Locate every blood parasite and identify its species.
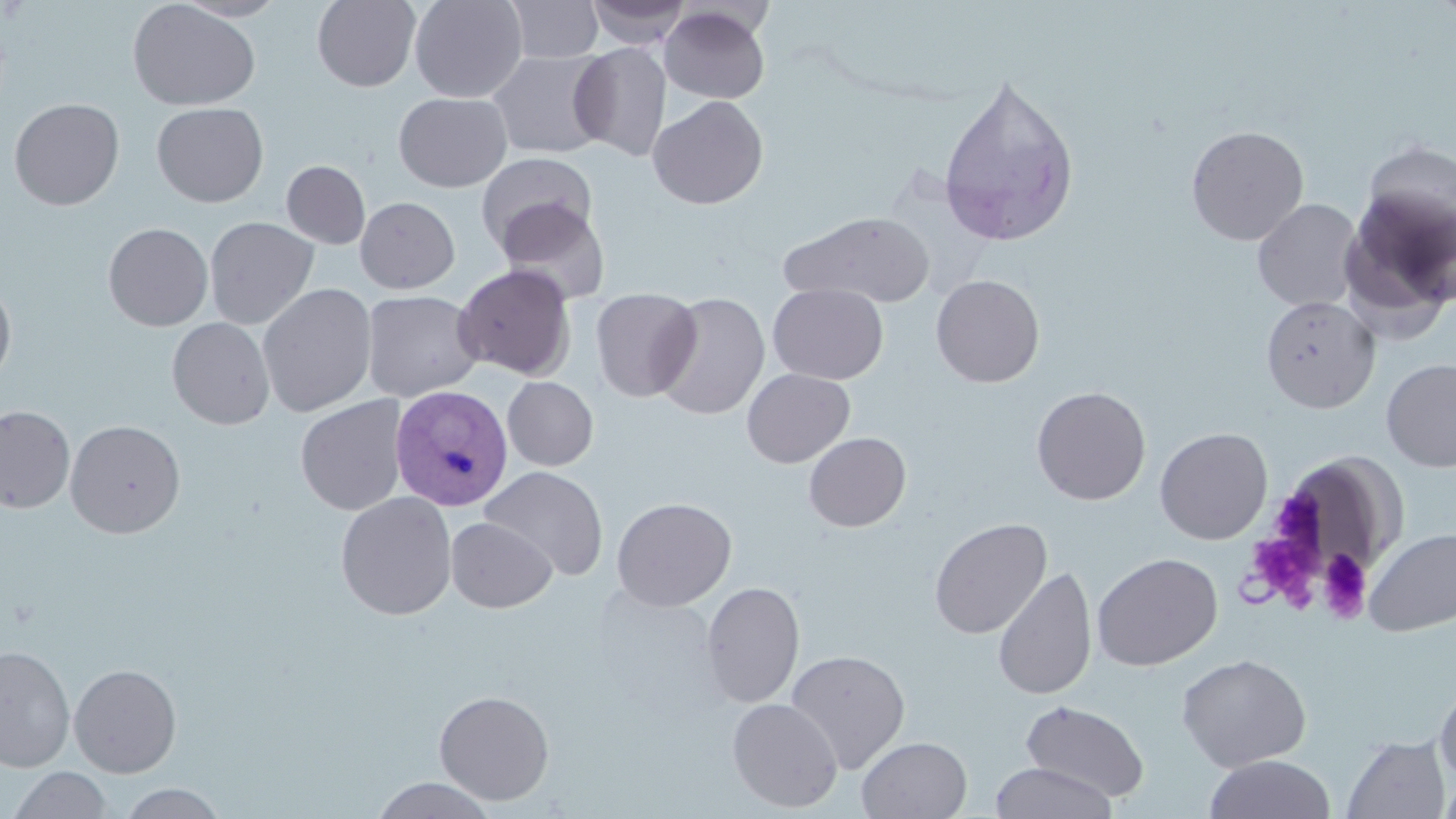

Approximate bounding boxes as (x1,y1)-(x2,y2) corner pairs in pixels.
Plasmodium vivax-infected red blood cells: (389,384)-(514,511).
No Plasmodium falciparum, Plasmodium ovale, Plasmodium malariae, Babesia divergens, or Trypanosoma brucei observed.

Platelet locations: (1260,488)-(1327,613), (1316,549)-(1373,621). Uninfected red blood cell locations: (127,0)-(261,111), (173,0)-(291,21), (312,0)-(420,91), (410,0)-(527,103), (504,0)-(604,63), (585,0)-(691,48), (660,6)-(770,104), (569,42)-(671,161), (486,49)-(611,158), (937,71)-(1080,248), (393,92)-(512,192), (648,95)-(768,210), (8,97)-(125,210), (151,102)-(269,207), (1186,125)-(1309,245), (1357,137)-(1456,248), (477,152)-(597,255), (281,160)-(370,249), (355,196)-(460,294), (495,198)-(610,305), (1252,198)-(1363,311), (780,210)-(935,308), (204,216)-(319,330), (103,223)-(213,331), (453,262)-(577,380), (931,274)-(1045,388), (0,280)-(17,389), (768,283)-(888,384), (257,284)-(377,417), (590,288)-(702,402), (361,290)-(483,402), (655,292)-(770,420), (1261,295)-(1380,413), (167,317)-(275,429), (1381,359)-(1456,472), (741,368)-(854,468), (502,376)-(599,471), (1031,386)-(1151,505), (295,395)-(408,516), (0,405)-(76,514), (65,419)-(186,539), (1155,427)-(1273,544), (803,431)-(911,532), (1292,447)-(1412,573), (478,465)-(609,581), (335,492)-(457,620), (611,497)-(737,611), (445,516)-(557,612), (928,517)-(1052,639), (1363,527)-(1456,637), (1092,552)-(1222,671), (992,566)-(1097,701), (700,581)-(805,709), (586,588)-(724,716), (0,644)-(75,772), (785,649)-(911,774), (1176,653)-(1312,771), (69,663)-(182,777), (1434,682)-(1456,785), (434,689)-(555,805), (727,698)-(843,813), (1020,699)-(1150,802), (1340,733)-(1451,819), (856,735)-(972,819), (1203,754)-(1336,819), (990,762)-(1116,819), (9,766)-(112,819), (1438,771)-(1456,819), (370,776)-(497,819), (119,783)-(228,818). Slide-level diagnosis: Plasmodium vivax. 1000x magnification. Light microscopy. May-Grünwald-Giemsa-stained preparation. Image is 1456×819 pixels. One field of a larger specimen. Thin blood smear.